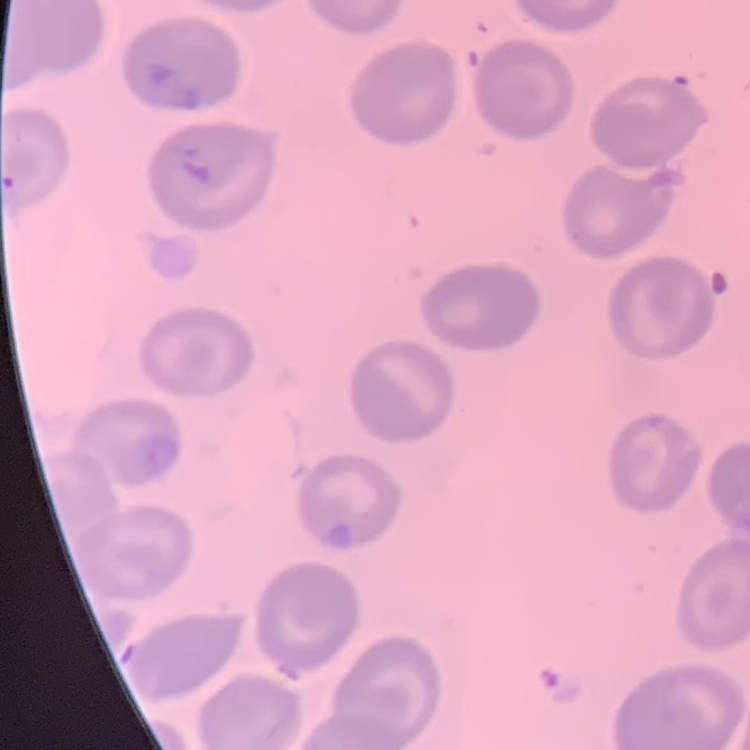

Summary:
  - Red blood cell morphology: no rouleaux formation
  - Preparation: thin blood smear
  - Image type: one tile cut from a larger photomicrograph
  - Stain: Field's or Giemsa